Comment on the morphology of the erythrocytes.
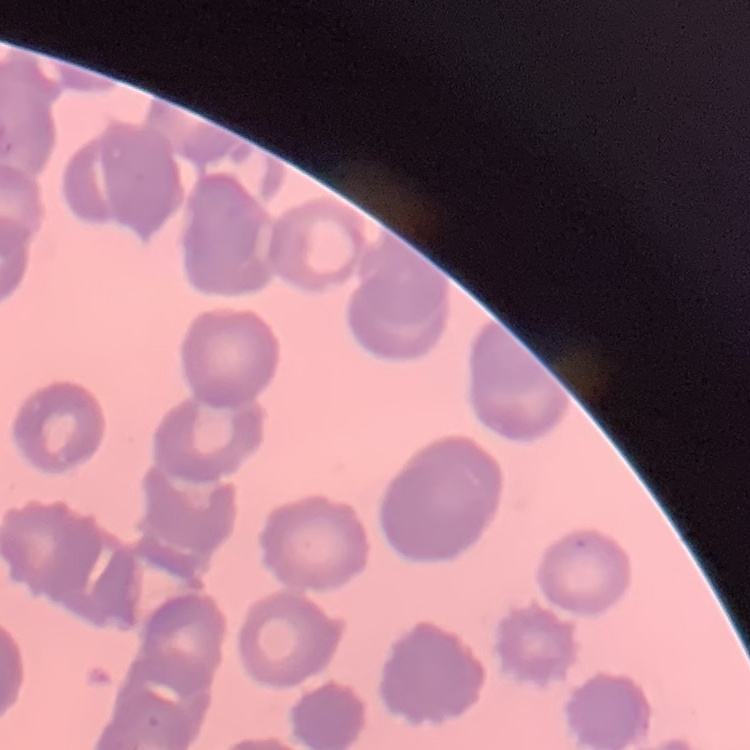

Rouleaux formation.

{
  "stain": "Field's or Giemsa",
  "preparation": "thin blood smear",
  "image_type": "square crop of a larger photomicrograph"
}